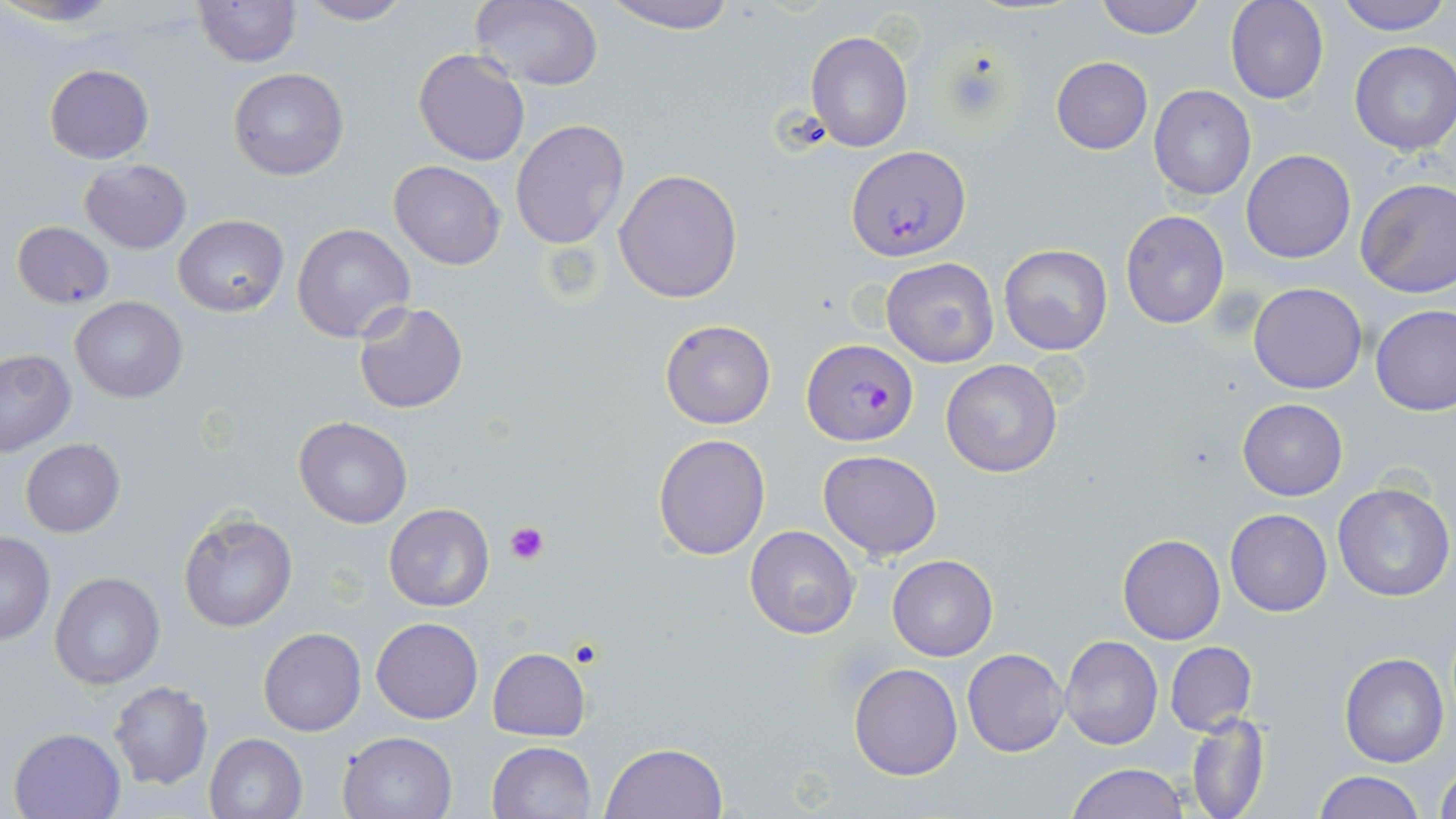
{
  "slide_level_diagnosis": "Plasmodium falciparum",
  "uninfected_red_blood_cell_locations": "approximate bounding boxes as (x1, y1, x2, y2) in pixels: (469, 0, 604, 90), (601, 0, 738, 34), (1095, 0, 1205, 39), (1226, 0, 1329, 104), (1333, 0, 1453, 36), (192, 1, 303, 68), (293, 1, 416, 26), (805, 31, 914, 151), (1349, 39, 1456, 156), (412, 47, 531, 166), (1051, 57, 1153, 154), (44, 64, 153, 163), (227, 67, 349, 181), (1149, 85, 1257, 201), (510, 119, 630, 249), (1241, 150, 1356, 263), (79, 158, 191, 254), (388, 161, 505, 269), (613, 168, 744, 303), (1354, 176, 1456, 300), (1120, 209, 1231, 329), (174, 214, 289, 317), (11, 221, 115, 308), (292, 223, 416, 345), (997, 243, 1114, 355), (881, 257, 999, 369), (1247, 283, 1368, 395), (70, 295, 188, 404), (352, 301, 469, 415), (1371, 306, 1456, 416), (661, 319, 776, 429), (0, 349, 75, 457), (940, 359, 1064, 477), (1238, 398, 1347, 500), (294, 416, 412, 529), (653, 433, 770, 560), (20, 438, 125, 538), (819, 450, 942, 559), (1331, 481, 1454, 602), (383, 503, 494, 613), (1224, 508, 1332, 617), (178, 511, 296, 633), (745, 527, 860, 640), (0, 532, 56, 644), (1117, 533, 1225, 645), (887, 554, 997, 660), (49, 570, 166, 690), (371, 617, 483, 723), (258, 628, 366, 737), (1060, 637, 1163, 750), (1165, 641, 1257, 736), (487, 648, 590, 741), (962, 648, 1069, 757), (1339, 651, 1449, 767), (848, 663, 963, 781), (108, 681, 213, 789), (1186, 711, 1270, 819), (8, 726, 127, 818), (336, 731, 459, 819), (204, 733, 307, 819), (487, 740, 596, 819), (600, 742, 729, 819), (1432, 759, 1456, 818), (1067, 763, 1188, 819), (1313, 771, 1426, 819)",
  "preparation": "thin blood smear",
  "modality": "optical microscopy",
  "magnification": "1000x",
  "platelet_locations": "approximate bounding boxes as (x1, y1, x2, y2) in pixels: (504, 521, 548, 564)",
  "image_size": "1456×819 pixels",
  "plasmodium_falciparum_infected_red_blood_cell_locations": "approximate bounding boxes as (x1, y1, x2, y2) in pixels: (847, 146, 970, 260), (801, 339, 916, 446)",
  "field_of_view": "single",
  "stain": "May-Grünwald-Giemsa"
}